Locate the red blood cells and classify each one as Plasmodium falciparum-infected, uninfected, or of indeterminate infection status.
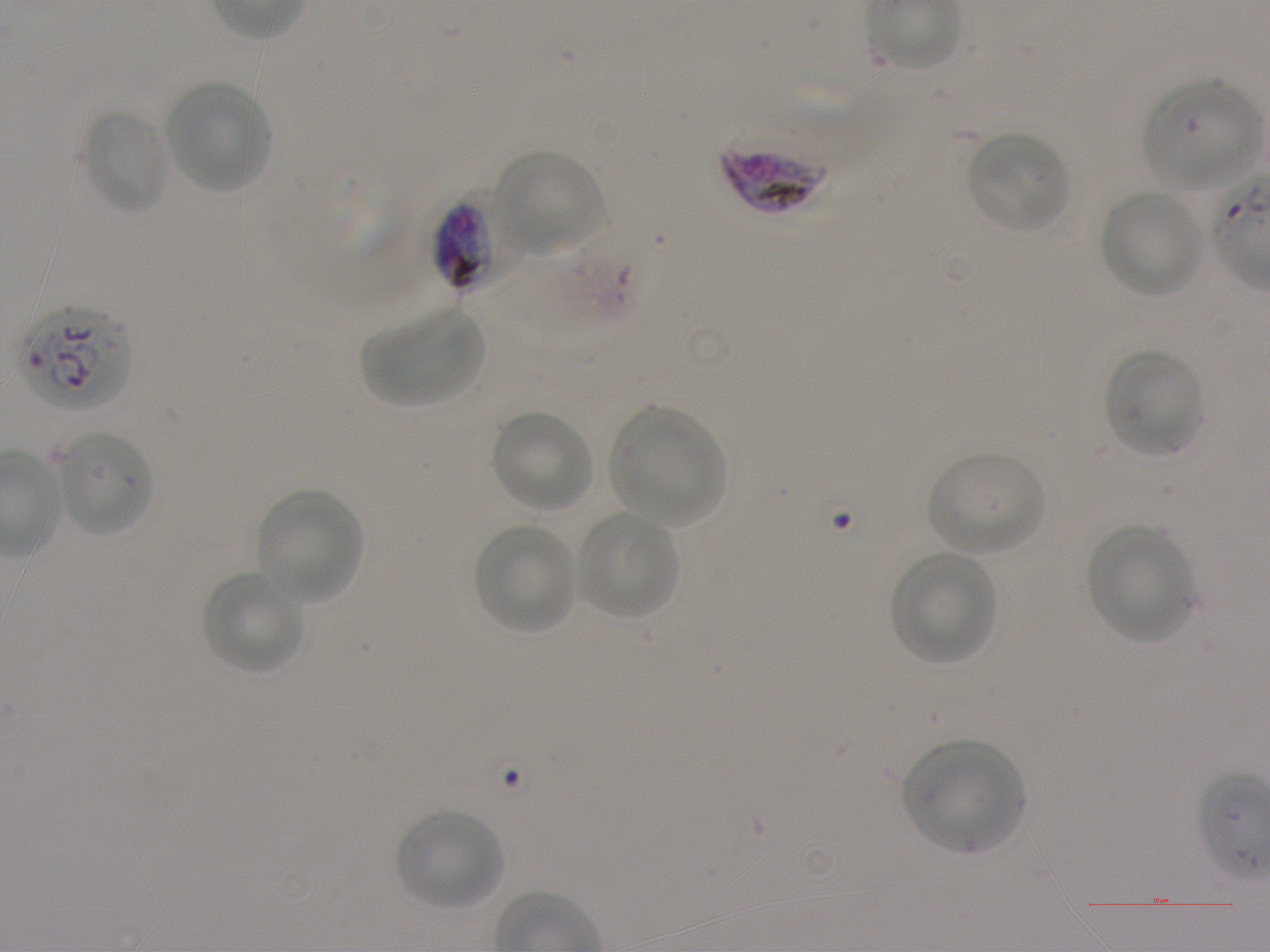

Approximate bounding boxes as [x1, y1, x2, y2] in pixels. Not every red blood cell is marked.
Infected red blood cells: [721, 146, 828, 214], [19, 302, 132, 411].
Red blood cells of indeterminate infection status: [1143, 78, 1261, 188], [436, 192, 525, 285], [554, 241, 646, 329].
Uninfected red blood cells: [165, 80, 272, 193], [81, 109, 171, 214], [967, 131, 1071, 233], [494, 150, 605, 254], [1100, 190, 1204, 297], [363, 307, 486, 407], [1105, 349, 1204, 457], [610, 405, 726, 527], [491, 410, 594, 514], [57, 430, 153, 537], [928, 450, 1047, 556], [257, 487, 364, 602], [577, 513, 678, 619], [471, 523, 576, 635], [1085, 525, 1192, 642], [889, 551, 997, 665], [201, 572, 306, 675], [903, 739, 1026, 855], [397, 809, 504, 910].

Giemsa stain. Thin blood smear. Image is 1270×952 pixels. Donor blood group A+. 100x objective under oil immersion, numerical aperture 1.25. Single field of view. Plasmodium falciparum strain NF54 in static in-vitro culture.